Name the parasite shown.
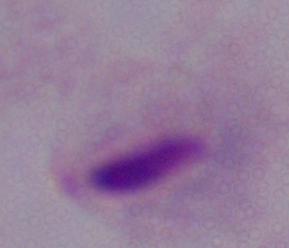
This is a trichomonad.

{
  "modality": "micrograph",
  "magnification": "1000x"
}